Report the malaria status.
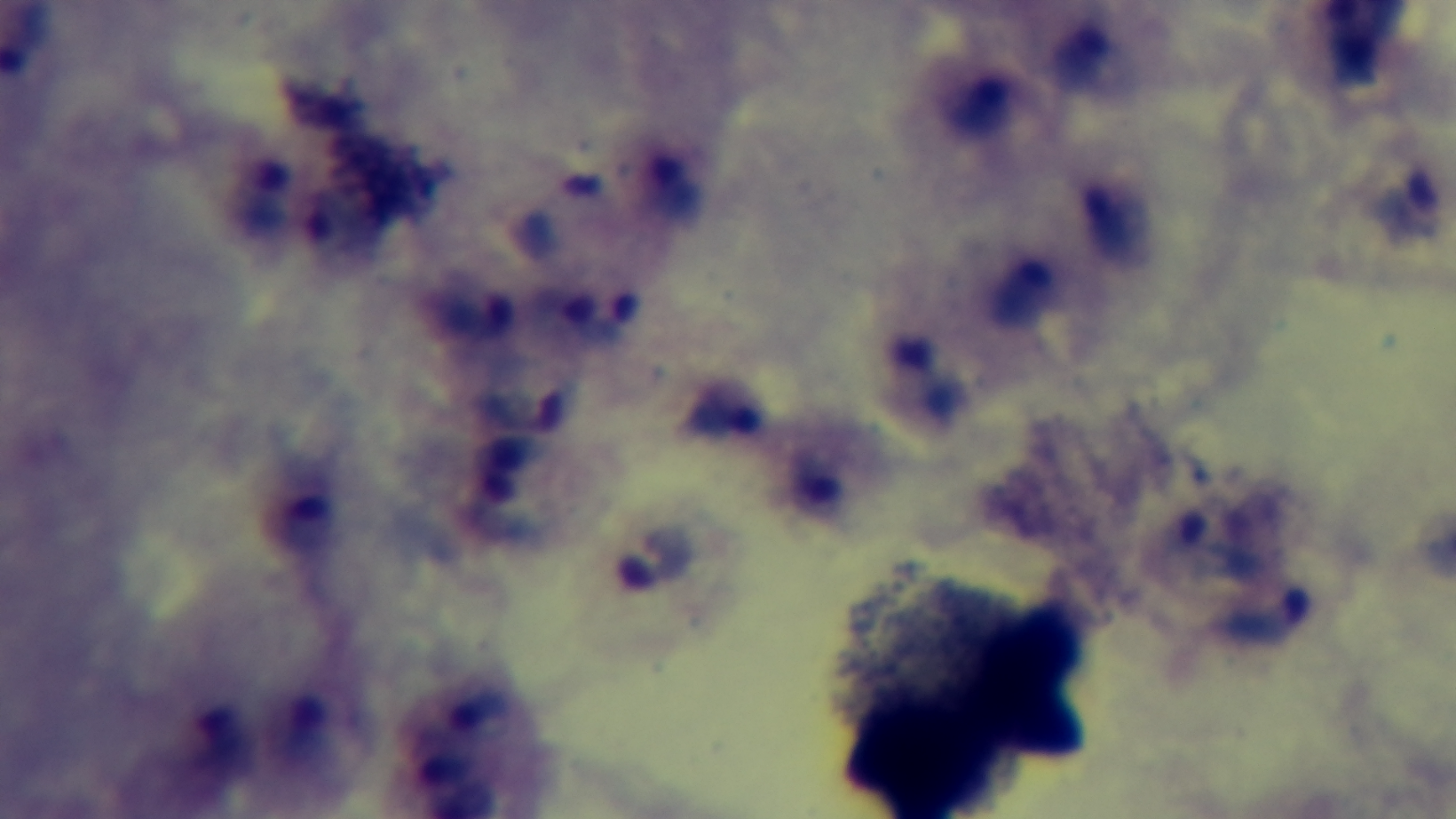

Infected.

Summary:
  - Preparation: thick blood film
  - Objective: 100x oil immersion
  - Modality: light microscopy
  - Field of view: one from the slide
  - Stain: Giemsa
  - Capture: mounted 4K digital camera